Name the cell type shown.
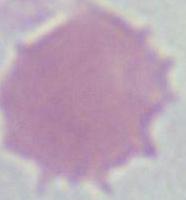
This is an erythrocyte.

Photomicrograph. Captured at 1000x magnification.